Report the malaria status of this cell.
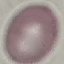
It is uninfected.

image_type: automatically extracted cell patch, resized to 64 × 64 pixels
stain: Giemsa
preparation: thin blood smear
capture: smartphone camera at the microscope eyepiece